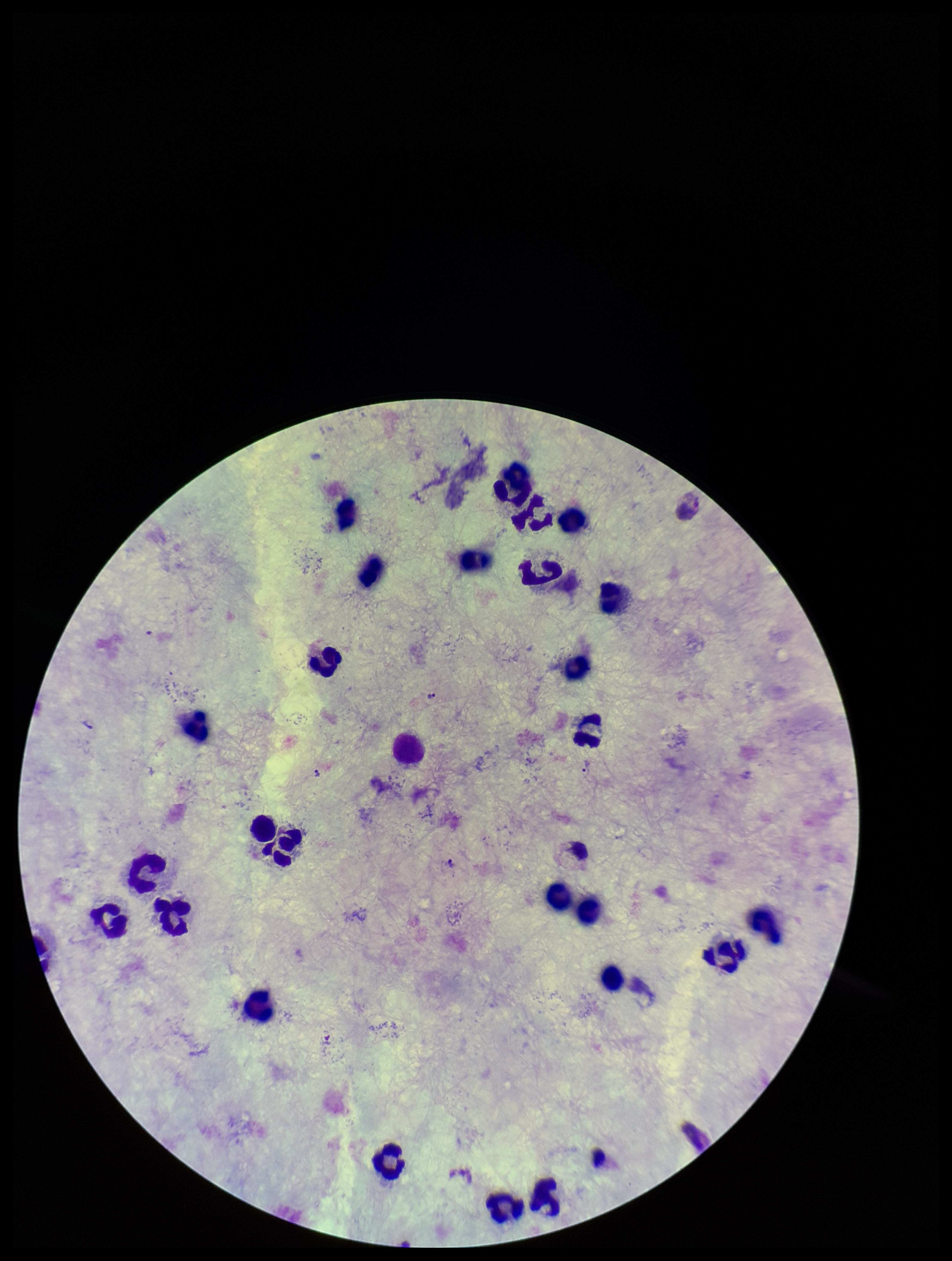
Parasite count: 3. Plasmodium parasites: detected. Giemsa stain. Leukocyte count: 27. Species reported for this patient: Plasmodium vivax. Patient malaria status: infected. Image is 952×1261 pixels. Photographed through the microscope eyepiece with a smartphone camera. Preparation: thick. One field from this slide.